Assess this cell for malaria.
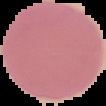

It is uninfected.

Image is 106×106 pixels. Segmented cell region on a black background. From a thin blood film.